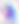
Toxoplasma gondii is seen. Photomicrograph. 400x magnification.